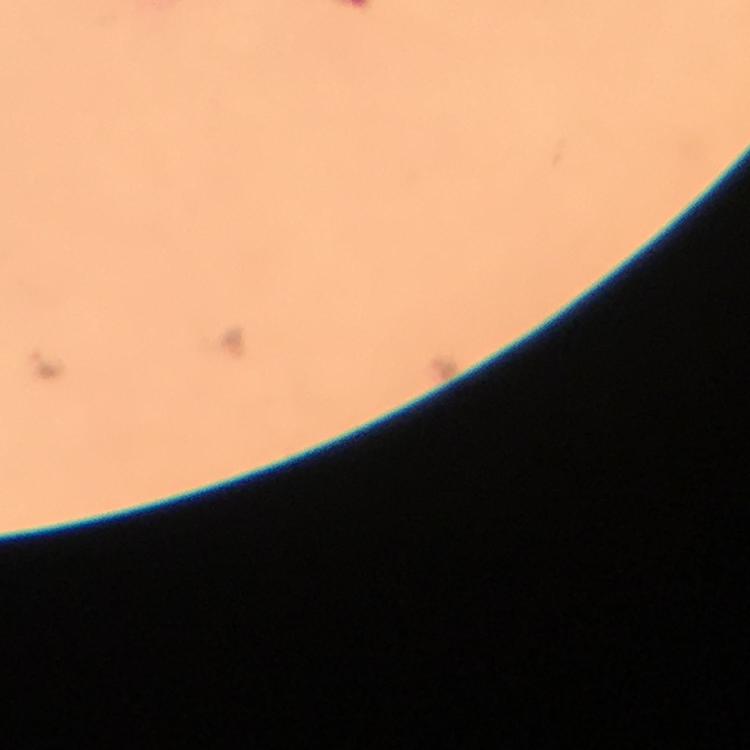
Approximate centers as [x, y] in pixels.
Summary:
  - Malaria parasite locations: [51, 363]
  - Image size: 750×750 pixels
  - Context: from a malaria diagnostic workup
  - Immersion oil: used
  - Preparation: thick blood smear
  - Capture: smartphone camera through the microscope
  - Magnification: 100x
  - Cropped from: a single field of view
  - Stain: Giemsa